Locate every Plasmodium falciparum parasite and give its life-cycle stage, and locate every leukocyte and any debris.
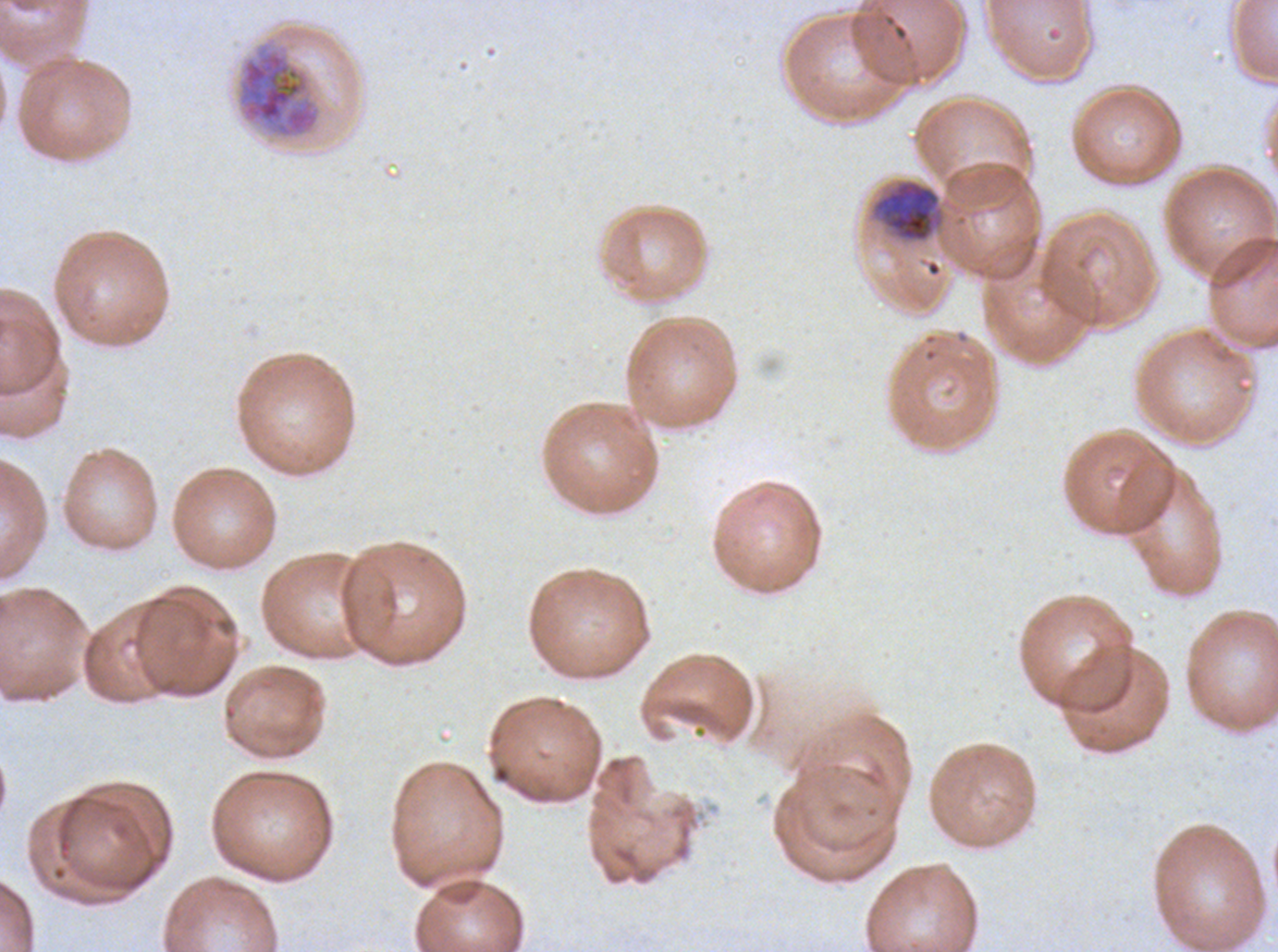
Approximate bounding boxes as (x1, y1, x2, y2) in pixels.
Late trophozoites: (871, 178, 945, 243).
Late schizonts: (237, 42, 322, 139).
No rings, late-ring/early-trophozoite forms, mid trophozoites, early schizonts, segmenters, gametocytes, leukocytes, or debris observed.

Giemsa-stained preparation. Life-cycle stages observed: late trophozoite, late schizont. A sub-image separated from a larger composite. Thin blood film. Image is 1278×952 pixels. Ex-vivo Plasmodium falciparum culture from a patient in The Gambia, grown for 24 to 48 hours.